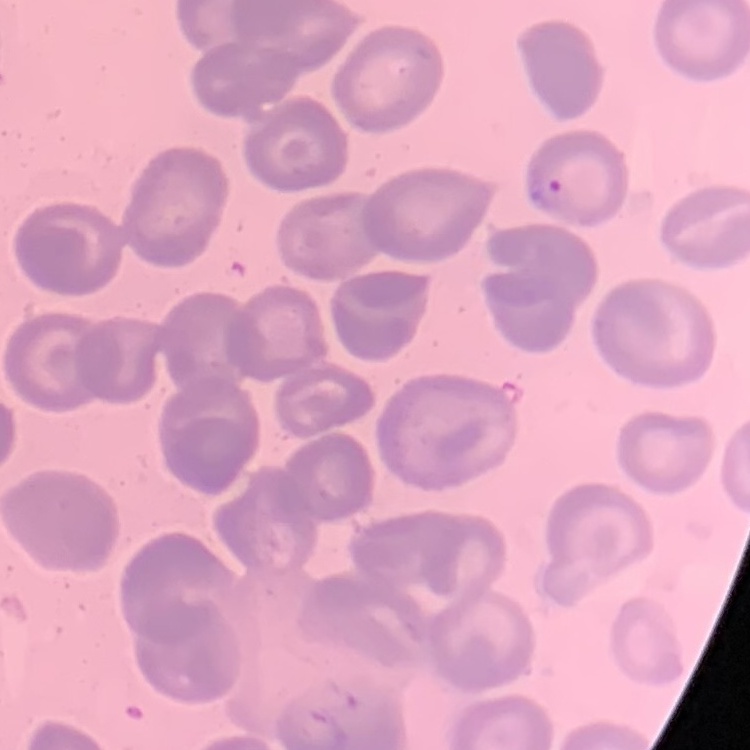

The red blood cells exhibit no rouleaux formation. Thin blood smear. One tile cut from a larger photomicrograph. Stained with either Field's or Giemsa.